State which cell type is depicted.
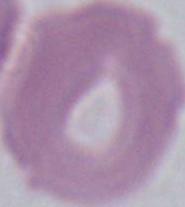

An erythrocyte.

magnification = 1000x
modality = photomicrograph